State the blood parasite species.
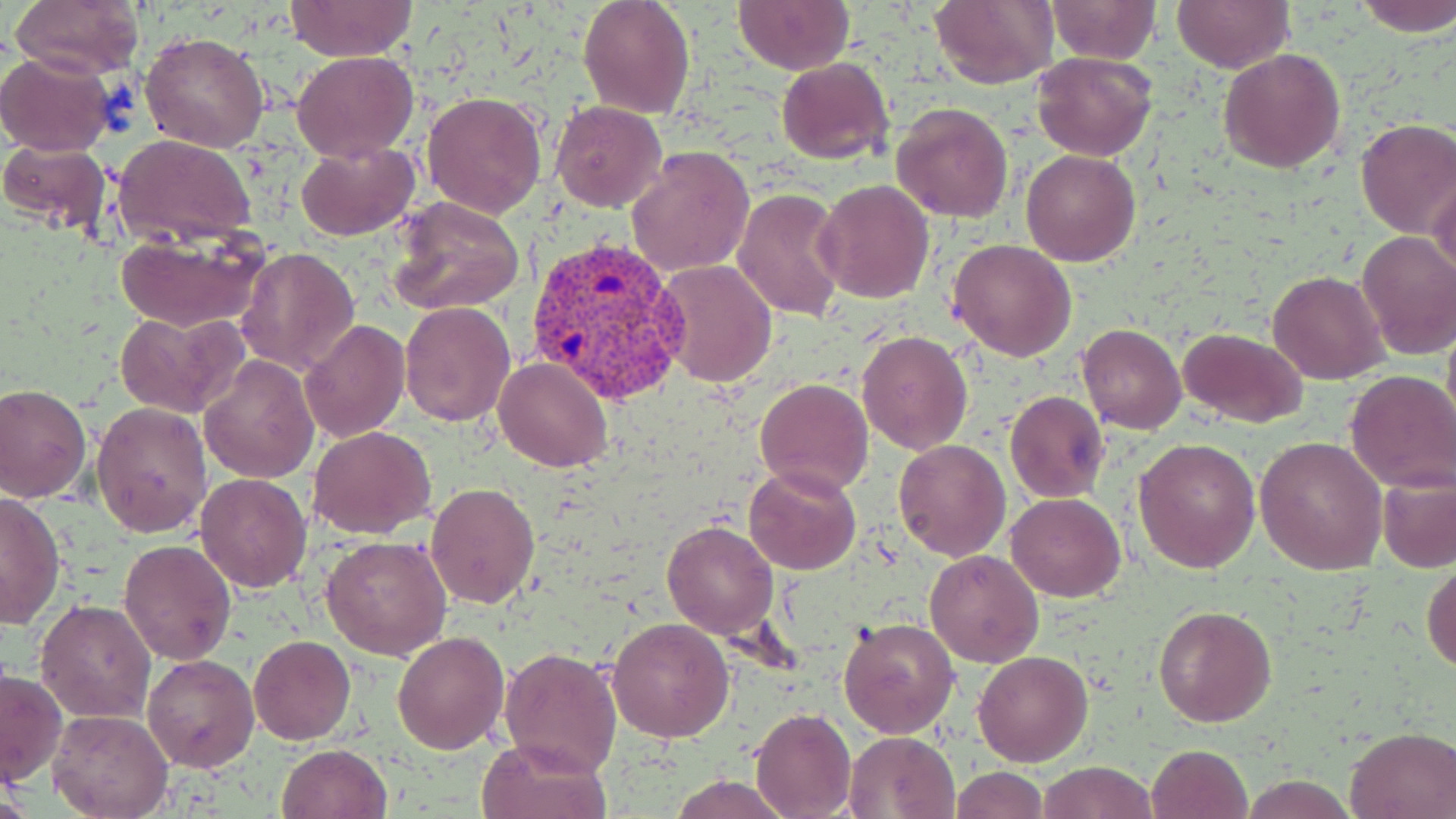

Plasmodium vivax.

preparation = thin blood film
uninfected red blood cell locations = approximate bounding boxes as [x1, y1, x2, y2] in pixels: [11, 0, 146, 80], [578, 0, 696, 120], [732, 0, 854, 74], [929, 0, 1057, 90], [1043, 0, 1163, 65], [1172, 0, 1293, 73], [1353, 0, 1456, 38], [284, 1, 418, 63], [140, 30, 272, 154], [1218, 48, 1347, 174], [291, 50, 420, 162], [1031, 50, 1157, 161], [0, 51, 118, 157], [776, 58, 893, 166], [421, 90, 547, 218], [552, 101, 667, 212], [891, 101, 1014, 223], [1354, 118, 1456, 238], [113, 135, 258, 243], [0, 140, 113, 236], [295, 140, 418, 239], [626, 145, 756, 277], [1020, 148, 1141, 266], [1426, 172, 1455, 279], [813, 178, 935, 303], [732, 188, 848, 322], [386, 197, 525, 316], [115, 230, 269, 332], [1356, 231, 1456, 359], [948, 238, 1077, 362], [236, 246, 360, 376], [655, 259, 778, 389], [1269, 271, 1387, 384], [400, 301, 516, 427], [113, 309, 249, 419], [300, 320, 410, 442], [1078, 322, 1186, 434], [1177, 326, 1308, 429], [855, 329, 973, 455], [200, 354, 318, 481], [494, 357, 612, 473], [1343, 370, 1456, 495], [755, 379, 873, 497], [0, 384, 92, 503], [1003, 391, 1109, 503], [91, 401, 213, 537], [308, 426, 436, 539], [894, 437, 1011, 560], [1132, 437, 1261, 575], [1256, 438, 1386, 574], [745, 464, 861, 575], [195, 473, 312, 593], [1378, 474, 1456, 573], [426, 482, 540, 608], [0, 490, 64, 629], [1007, 493, 1125, 601], [662, 520, 778, 639], [321, 534, 453, 661], [119, 539, 235, 666], [925, 549, 1044, 667], [1422, 559, 1455, 674], [37, 599, 157, 722], [1153, 605, 1277, 728], [607, 616, 735, 741], [838, 617, 959, 738], [391, 630, 510, 755], [249, 635, 355, 743], [499, 646, 622, 778], [973, 649, 1092, 766], [142, 654, 261, 773], [1, 666, 66, 789], [750, 708, 857, 818], [49, 709, 172, 819], [1345, 727, 1456, 818], [844, 732, 961, 819], [475, 736, 612, 819], [275, 743, 392, 818], [1145, 744, 1253, 819], [1038, 759, 1160, 818], [950, 766, 1048, 819], [666, 775, 796, 819], [1241, 775, 1358, 817]
field of view = one of a larger specimen
modality = optical microscopy
magnification = 1000x
image size = 1456×819 pixels
stain = May-Grünwald-Giemsa
Plasmodium vivax-infected red blood cell locations = approximate bounding boxes as [x1, y1, x2, y2] in pixels: [522, 235, 691, 409]